Assess this cell for malaria.
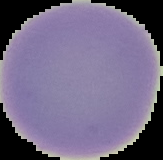
Uninfected.

image type = segmented cell region with the area outside set to black
preparation = thin blood smear
image size = 163×160 pixels